State which parasite is depicted.
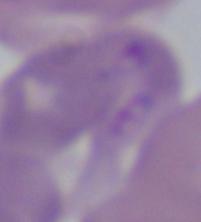
Babesia.

magnification = 1000x
modality = micrograph